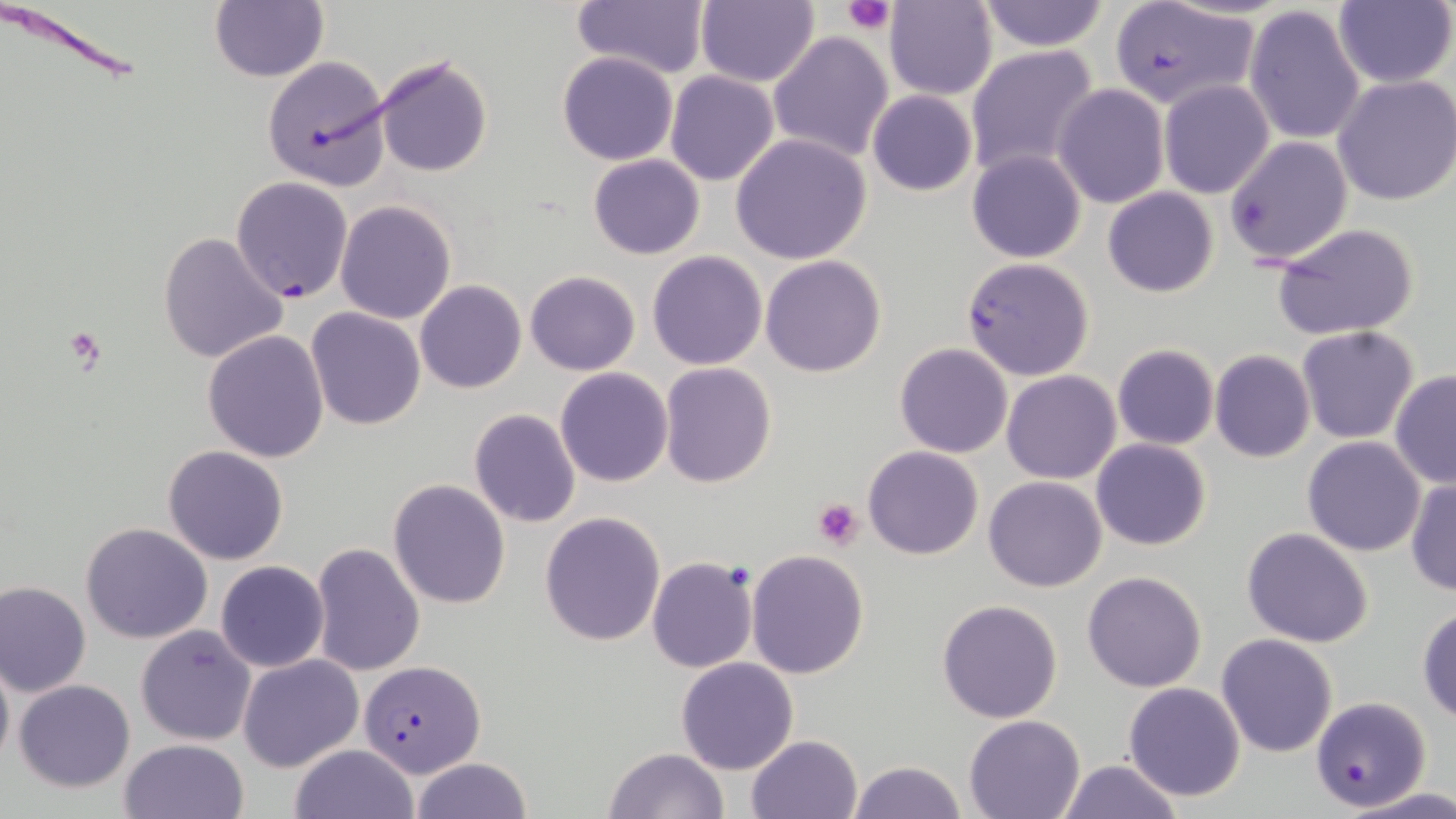

slide-level diagnosis = Plasmodium falciparum
image size = 1456×819 pixels
platelet locations = approximate bounding boxes as [x1, y1, x2, y2] in pixels: [845, 0, 895, 33], [64, 329, 110, 371], [812, 499, 864, 549]
stain = May-Grünwald-Giemsa
field of view = single
preparation = thin blood film
Plasmodium falciparum-infected red blood cell locations = approximate bounding boxes as [x1, y1, x2, y2] in pixels: [1107, 2, 1262, 112], [231, 177, 353, 303], [960, 257, 1095, 381], [358, 659, 483, 777], [1311, 698, 1428, 812]
uninfected red blood cell locations = approximate bounding boxes as [x1, y1, x2, y2] in pixels: [570, 0, 713, 81], [696, 0, 819, 87], [1333, 0, 1455, 88], [884, 1, 997, 100], [975, 1, 1110, 51], [209, 2, 328, 82], [1243, 4, 1367, 146], [768, 30, 894, 163], [965, 45, 1100, 178], [557, 51, 678, 165], [374, 53, 494, 177], [262, 56, 392, 190], [665, 71, 779, 185], [1332, 76, 1456, 207], [1158, 80, 1274, 199], [1053, 83, 1171, 209], [867, 89, 978, 196], [731, 134, 873, 265], [1224, 136, 1353, 265], [966, 149, 1087, 263], [588, 153, 705, 259], [1102, 187, 1219, 297], [336, 200, 456, 323], [1270, 222, 1421, 342], [158, 230, 289, 365], [647, 250, 766, 369], [760, 255, 887, 377], [525, 270, 640, 375], [415, 281, 526, 394], [306, 306, 427, 430], [1296, 326, 1419, 444], [202, 331, 329, 462], [895, 343, 1012, 458], [1112, 344, 1219, 450], [1210, 350, 1315, 463], [660, 363, 777, 486], [555, 366, 673, 486], [1002, 370, 1121, 484], [1389, 370, 1456, 489], [468, 408, 580, 527], [1301, 436, 1426, 556], [1090, 438, 1213, 551], [162, 445, 290, 565], [862, 446, 984, 560], [983, 475, 1107, 592], [1405, 478, 1455, 596], [389, 479, 510, 610], [540, 511, 667, 648], [81, 522, 213, 644], [1241, 526, 1375, 648], [309, 543, 426, 677], [746, 550, 869, 679], [647, 556, 757, 673], [215, 560, 329, 672], [1082, 570, 1208, 693], [1, 580, 91, 696], [164, 584, 288, 720], [936, 599, 1064, 722], [1416, 604, 1456, 726], [135, 624, 256, 745], [1215, 633, 1340, 758], [0, 653, 13, 775], [237, 653, 363, 771], [676, 657, 799, 774], [13, 679, 136, 792], [1122, 682, 1246, 802], [964, 713, 1086, 817], [746, 734, 863, 819], [119, 738, 251, 819], [290, 744, 416, 819], [604, 746, 729, 819], [411, 756, 531, 819], [1057, 759, 1185, 818], [847, 760, 966, 819], [1339, 788, 1456, 819]
magnification = 1000x
modality = optical microscopy